Report the malaria status of this cell.
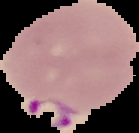

Parasitized.

image size = 139×133 pixels
image type = segmented cell region on a black background
preparation = thin blood smear